Locate every Plasmodium parasite.
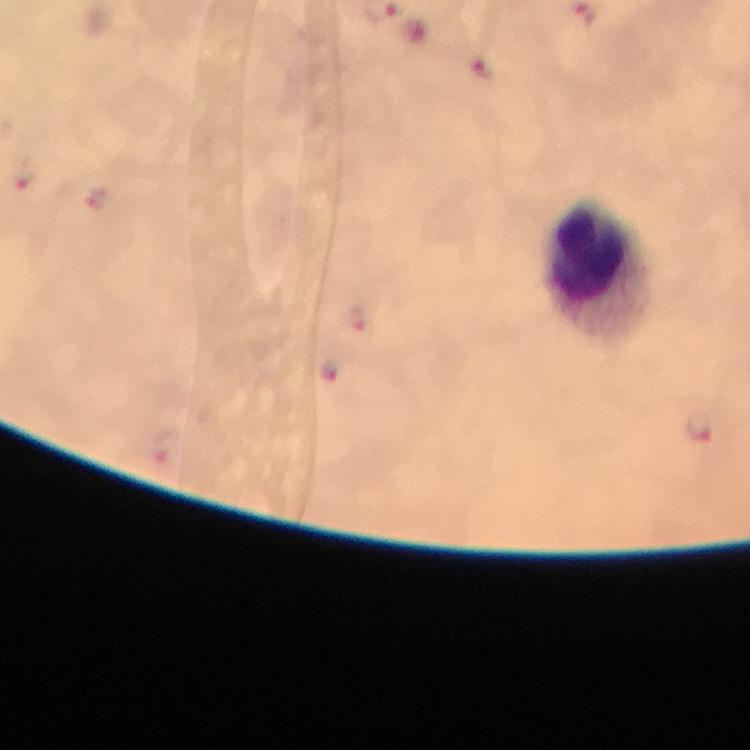

Approximate centers as (x, y) in pixels.
Plasmodium parasites: (482, 69), (25, 177), (94, 197), (355, 318), (328, 370), (701, 426).

Summary:
  - Leukocyte locations: (600, 267)
  - Capture: smartphone mounted on the microscope
  - Preparation: thick blood smear
  - Cropped from: a single field of view
  - Immersion oil: used
  - Stain: Giemsa
  - Magnification: 100x
  - Image size: 750×750 pixels
  - Context: from a diagnostic examination for malaria